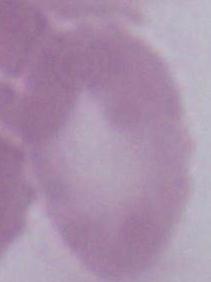

Summary:
  - Identification: red blood cell
  - Magnification: 1000x
  - Modality: photomicrograph